Outline each Plasmodium falciparum-infected red blood cell.
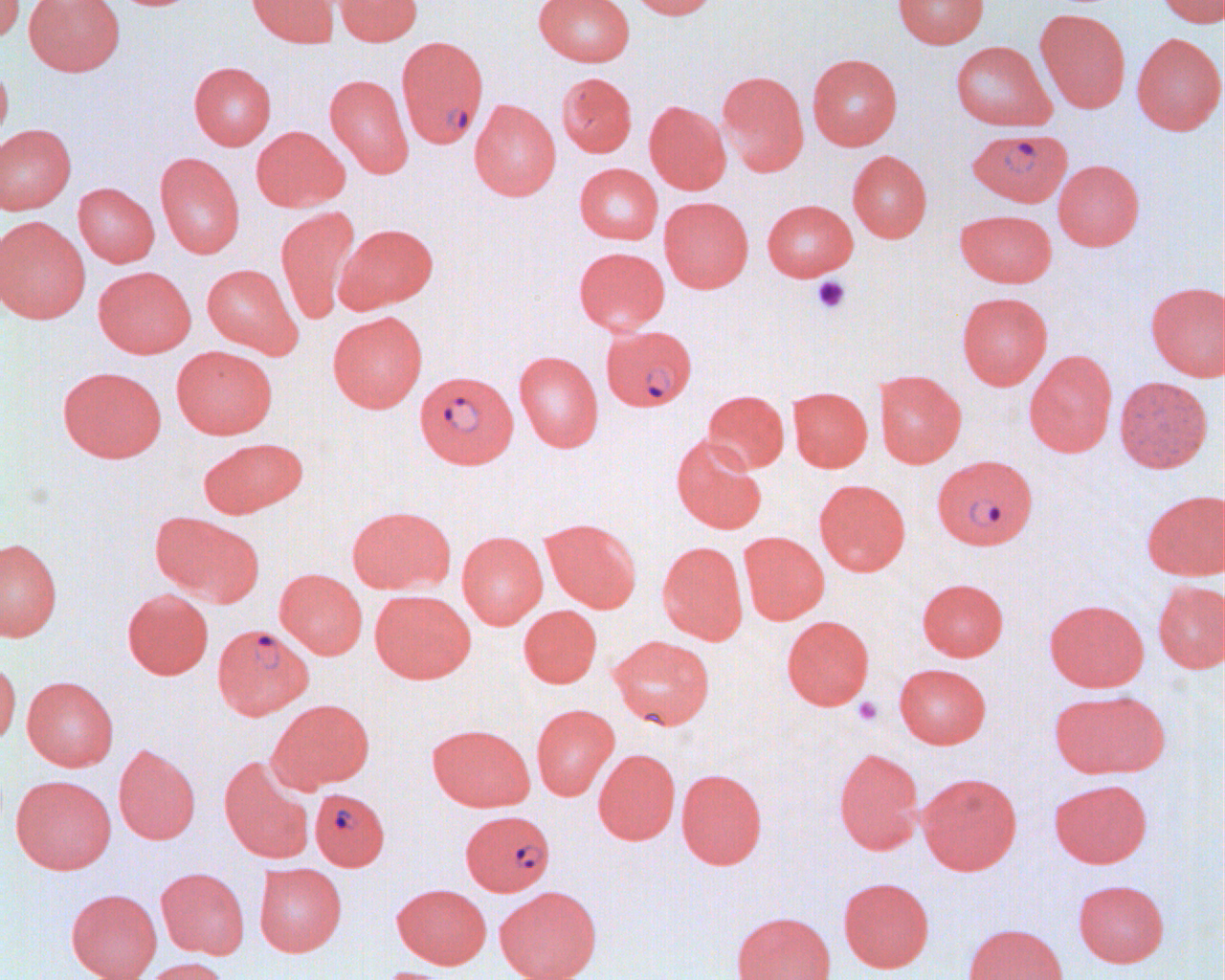
Approximate bounding boxes as [x1, y1, x2, y2] in pixels.
Plasmodium falciparum-infected red blood cells: [396, 35, 489, 148], [968, 128, 1072, 207], [603, 327, 698, 414], [414, 370, 518, 468], [931, 453, 1038, 550], [212, 624, 312, 720], [310, 788, 389, 870], [460, 810, 555, 896].

{
  "slide_level_diagnosis": "Plasmodium falciparum",
  "image_size": "1225×980 pixels",
  "platelet_locations": "approximate bounding boxes as [x1, y1, x2, y2] in pixels: [810, 276, 851, 315], [852, 697, 883, 726]",
  "field_of_view": "one of a larger specimen",
  "modality": "optical microscopy",
  "preparation": "thin blood smear",
  "magnification": "1000x",
  "uninfected_red_blood_cell_locations": "approximate bounding boxes as [x1, y1, x2, y2] in pixels: [0, 0, 25, 46], [24, 0, 125, 76], [247, 0, 338, 47], [334, 0, 422, 45], [535, 0, 635, 66], [628, 0, 720, 20], [892, 0, 989, 48], [1155, 0, 1224, 27], [1035, 9, 1130, 112], [1131, 33, 1224, 135], [951, 40, 1056, 130], [808, 53, 902, 150], [0, 62, 13, 149], [189, 62, 276, 149], [717, 71, 809, 176], [556, 72, 637, 157], [324, 73, 414, 178], [469, 99, 561, 200], [644, 100, 731, 194], [0, 123, 76, 214], [251, 125, 349, 212], [848, 150, 932, 242], [155, 152, 245, 259], [1053, 159, 1145, 250], [574, 163, 663, 244], [73, 183, 160, 267], [659, 196, 753, 292], [762, 199, 858, 281], [276, 206, 360, 324], [955, 209, 1057, 287], [0, 216, 90, 323], [336, 223, 439, 312], [573, 246, 670, 335], [202, 263, 302, 358], [93, 266, 196, 358], [1145, 281, 1225, 381], [956, 292, 1053, 389], [328, 312, 427, 412], [171, 346, 277, 439], [1024, 350, 1117, 457], [514, 351, 603, 452], [57, 366, 167, 462], [874, 370, 966, 467], [1114, 376, 1212, 473], [787, 386, 873, 472], [702, 390, 789, 473], [671, 435, 767, 534], [198, 437, 308, 518], [814, 479, 911, 575], [1142, 489, 1224, 581], [347, 505, 454, 595], [150, 513, 261, 602], [540, 518, 642, 613], [457, 531, 547, 629], [738, 531, 829, 625], [0, 536, 62, 641], [657, 541, 748, 644], [275, 569, 367, 659], [917, 577, 1009, 661], [1152, 580, 1225, 673], [122, 588, 214, 679], [369, 589, 476, 683], [1044, 598, 1149, 692], [519, 605, 602, 688], [781, 615, 875, 709], [608, 635, 716, 730], [0, 659, 21, 747], [894, 663, 991, 749], [22, 676, 118, 771], [1049, 689, 1169, 779], [270, 699, 374, 791], [531, 704, 619, 800], [427, 723, 535, 812], [113, 743, 200, 844], [593, 748, 680, 844], [833, 748, 923, 854], [219, 755, 315, 863], [676, 768, 767, 869], [917, 772, 1022, 875], [11, 774, 116, 874], [1049, 778, 1152, 868], [254, 863, 347, 956], [156, 867, 250, 959], [838, 877, 935, 972], [1073, 879, 1170, 967], [391, 883, 492, 968], [495, 886, 601, 980], [66, 888, 162, 980], [731, 910, 836, 980], [962, 923, 1069, 980], [140, 957, 229, 980], [371, 967, 457, 980]"
}